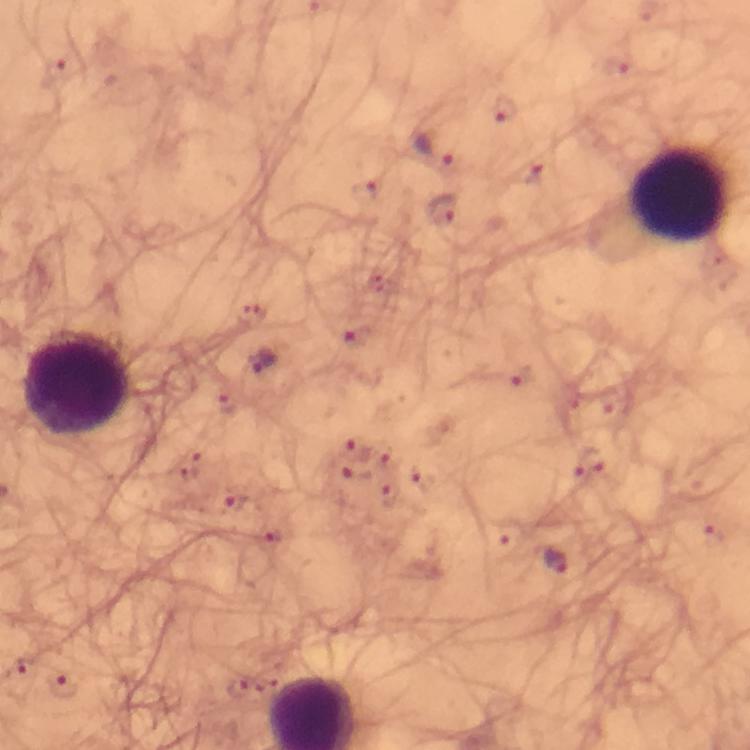 Approximate object centers, in pixels from the top-left corner. Malaria parasite locations: (x=504, y=108), (x=434, y=147), (x=442, y=210), (x=261, y=362), (x=353, y=448), (x=386, y=457), (x=355, y=473), (x=392, y=495), (x=231, y=503), (x=270, y=532), (x=556, y=562), (x=62, y=686), (x=234, y=687). Leukocyte locations: (x=679, y=192), (x=76, y=383). From a diagnostic examination for malaria. Image is 750×750 pixels. Immersion oil was used. Photographed through the microscope with a smartphone camera. Giemsa-stained preparation. Thick blood smear. A crop from one field of view. At 100x magnification.